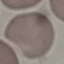
Summary:
  - Malaria status: uninfected
  - Preparation: thin blood film
  - Image type: automatically extracted cell patch, resized to 64 × 64 pixels
  - Stain: Giemsa
  - Capture: smartphone through the microscope eyepiece